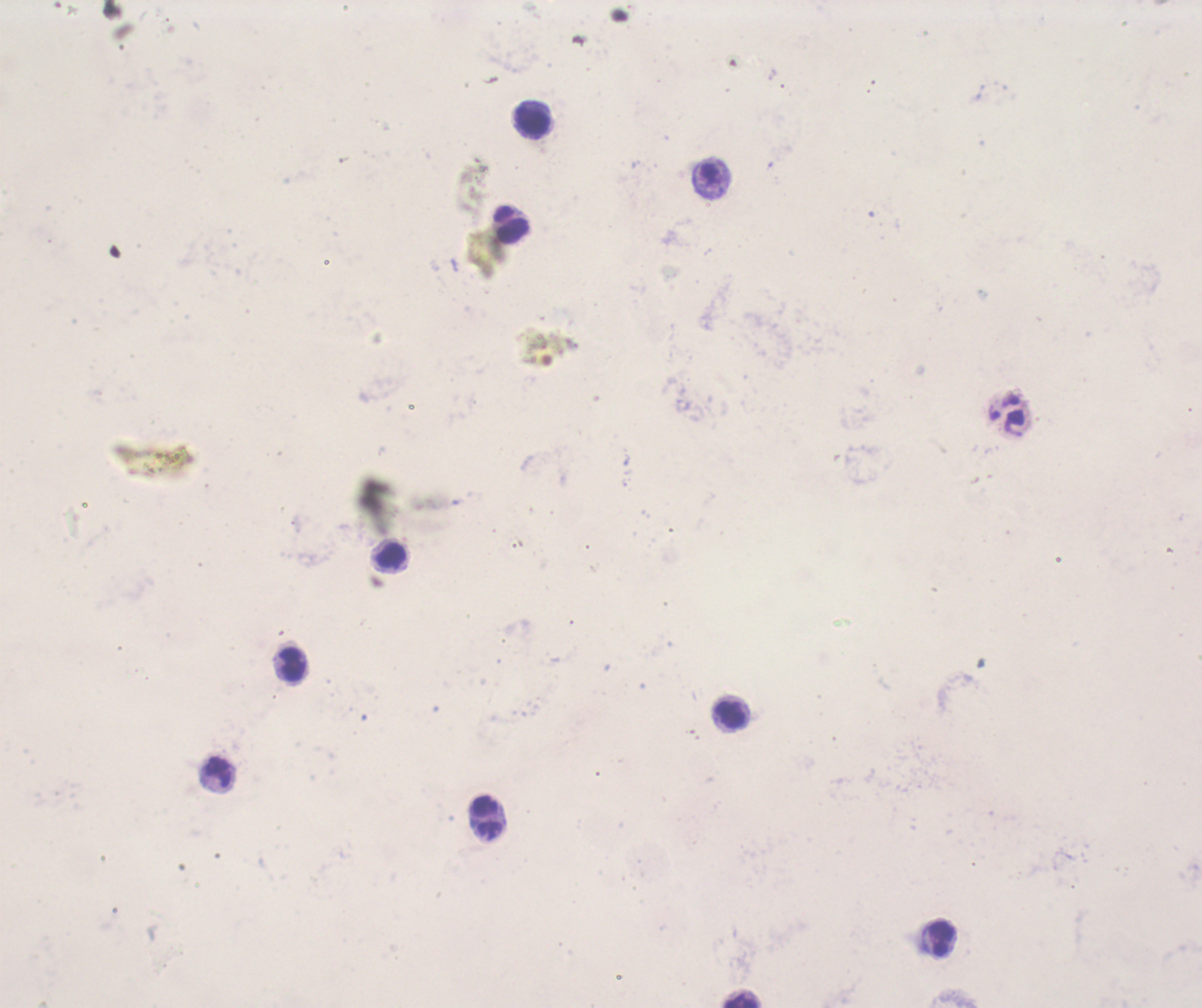
Approximate centers as {x, y} in pixels. Leukocyte locations: {533, 121}, {510, 223}, {392, 556}, {292, 664}, {731, 715}, {487, 818}, {941, 939}, {741, 1000}. 100x magnification. Result: no Plasmodium parasites detected. Coloration quality: bad. Romanowsky-stained preparation. Previously used in an actual diagnosis. Thick smear of blood. Single field of view. Background quality: poor. Image is 1202×1008 pixels.